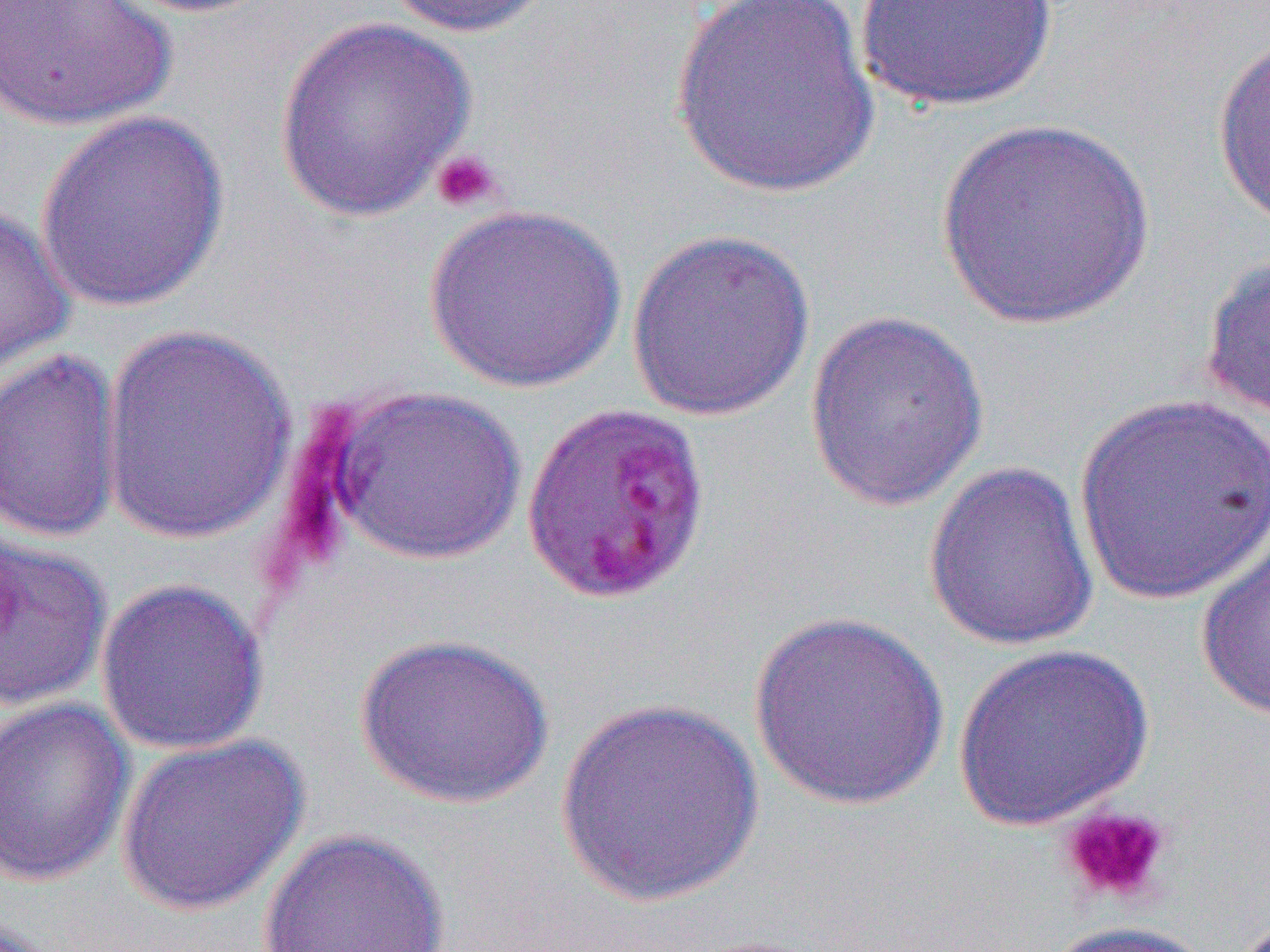

Approximate bounding boxes as named x1/y1/x2/y2 corners in pixels. Uninfected red blood cell locations: (x1=0, y1=0, x2=177, y2=132), (x1=110, y1=0, x2=282, y2=18), (x1=379, y1=0, x2=557, y2=37), (x1=667, y1=0, x2=882, y2=199), (x1=854, y1=0, x2=1060, y2=112), (x1=272, y1=17, x2=478, y2=220), (x1=1212, y1=29, x2=1270, y2=235), (x1=34, y1=110, x2=232, y2=314), (x1=934, y1=115, x2=1155, y2=331), (x1=0, y1=200, x2=75, y2=379), (x1=425, y1=204, x2=627, y2=393), (x1=625, y1=228, x2=817, y2=422), (x1=1199, y1=252, x2=1270, y2=420), (x1=803, y1=309, x2=991, y2=512), (x1=98, y1=321, x2=299, y2=545), (x1=0, y1=348, x2=124, y2=543), (x1=322, y1=384, x2=528, y2=565), (x1=1073, y1=393, x2=1269, y2=605), (x1=923, y1=459, x2=1100, y2=652), (x1=1195, y1=524, x2=1270, y2=721), (x1=1, y1=528, x2=112, y2=715), (x1=95, y1=577, x2=270, y2=756), (x1=748, y1=609, x2=950, y2=811), (x1=354, y1=632, x2=554, y2=810), (x1=953, y1=643, x2=1155, y2=832), (x1=0, y1=696, x2=135, y2=888), (x1=554, y1=696, x2=765, y2=908), (x1=115, y1=734, x2=310, y2=917), (x1=257, y1=827, x2=450, y2=951), (x1=1042, y1=920, x2=1219, y2=951). Platelet locations: (x1=430, y1=149, x2=503, y2=213), (x1=1058, y1=803, x2=1172, y2=908). Slide-level diagnosis: Plasmodium falciparum. 1000x magnification. Thin blood film. Image is 1270×952 pixels. One field of a larger specimen. Optical microscopy.